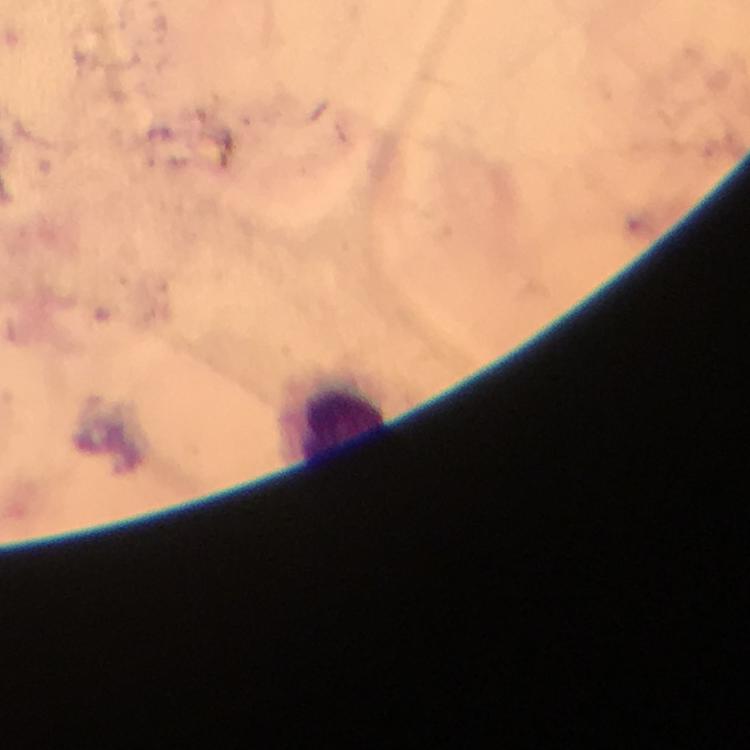

malaria parasites = none detected
preparation = thick smear
capture = smartphone photograph through a microscope
context = from a malaria diagnostic workup
cropped from = one field of view
stain = Giemsa
leukocyte locations = approximate centers as [x, y] in pixels: [341, 420]
immersion oil = used
magnification = 100x
image size = 750×750 pixels